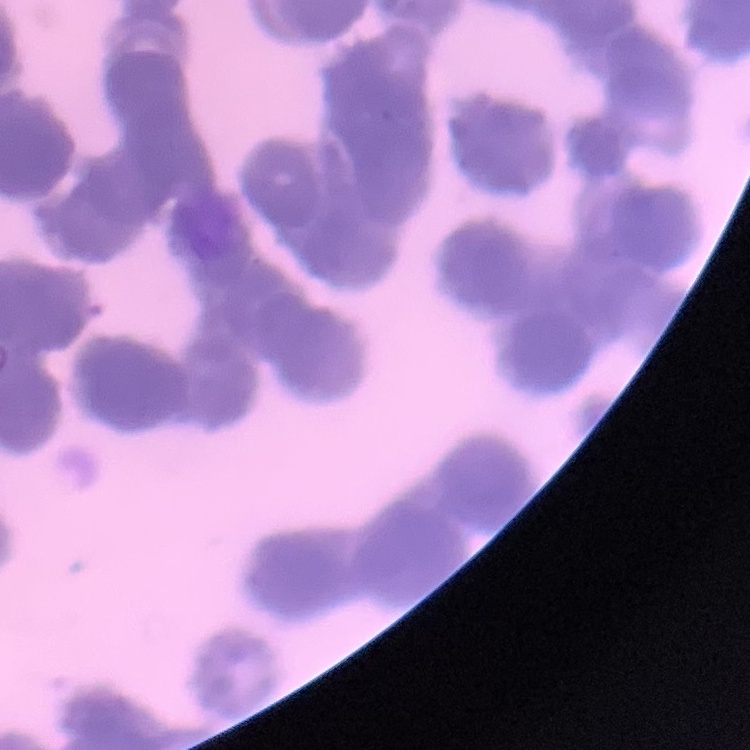

Summary:
  - Erythrocyte morphology: rouleaux formation
  - Image type: one tile cut from a larger photomicrograph
  - Stain: Field's or Giemsa
  - Preparation: thin peripheral smear